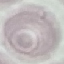 Malaria status: uninfected. Giemsa-stained preparation. Cell patch, automatically extracted from a larger field of view and resized to 64 × 64 pixels. Acquired by smartphone through the microscope eyepiece. Thin blood film.